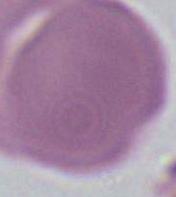 An erythrocyte is shown. Photomicrograph. 1000x magnification.